Report the malaria status of this cell.
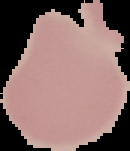

It is uninfected.

{
  "image_size": "130×151 pixels",
  "preparation": "thin blood film",
  "image_type": "cell region segmented out of the field of view; surrounding area masked to black"
}